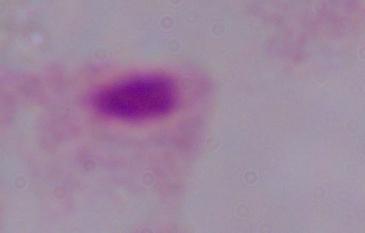

Summary:
  - Modality: photomicrograph
  - Identification: trichomonad
  - Magnification: 1000x